Classify this cell by malaria status.
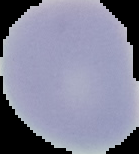

Uninfected.

The area outside the segmented cell region is set to black. Image is 139×154 pixels. From a thin blood film.